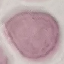

{
  "malaria_status": "uninfected",
  "image_type": "cell patch, automatically extracted from a larger field of view and resized to 64 × 64 pixels",
  "stain": "Giemsa",
  "preparation": "thin blood smear",
  "capture": "smartphone camera at the microscope eyepiece"
}